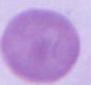 Photomicrograph. A red blood cell is shown. 1000x magnification.